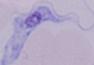
Summary:
  - Identification: trypanosome
  - Magnification: 1000x
  - Modality: micrograph